State which parasite is depicted.
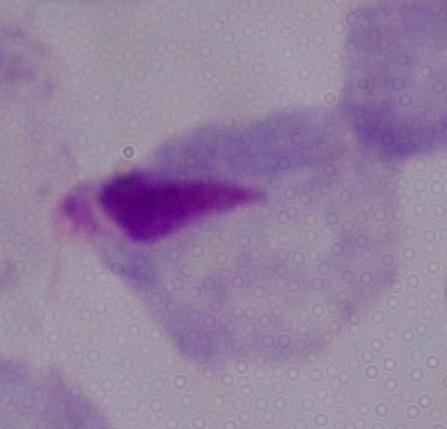

A trichomonad.

modality = photomicrograph
magnification = 1000x